Assess for Plasmodium parasites.
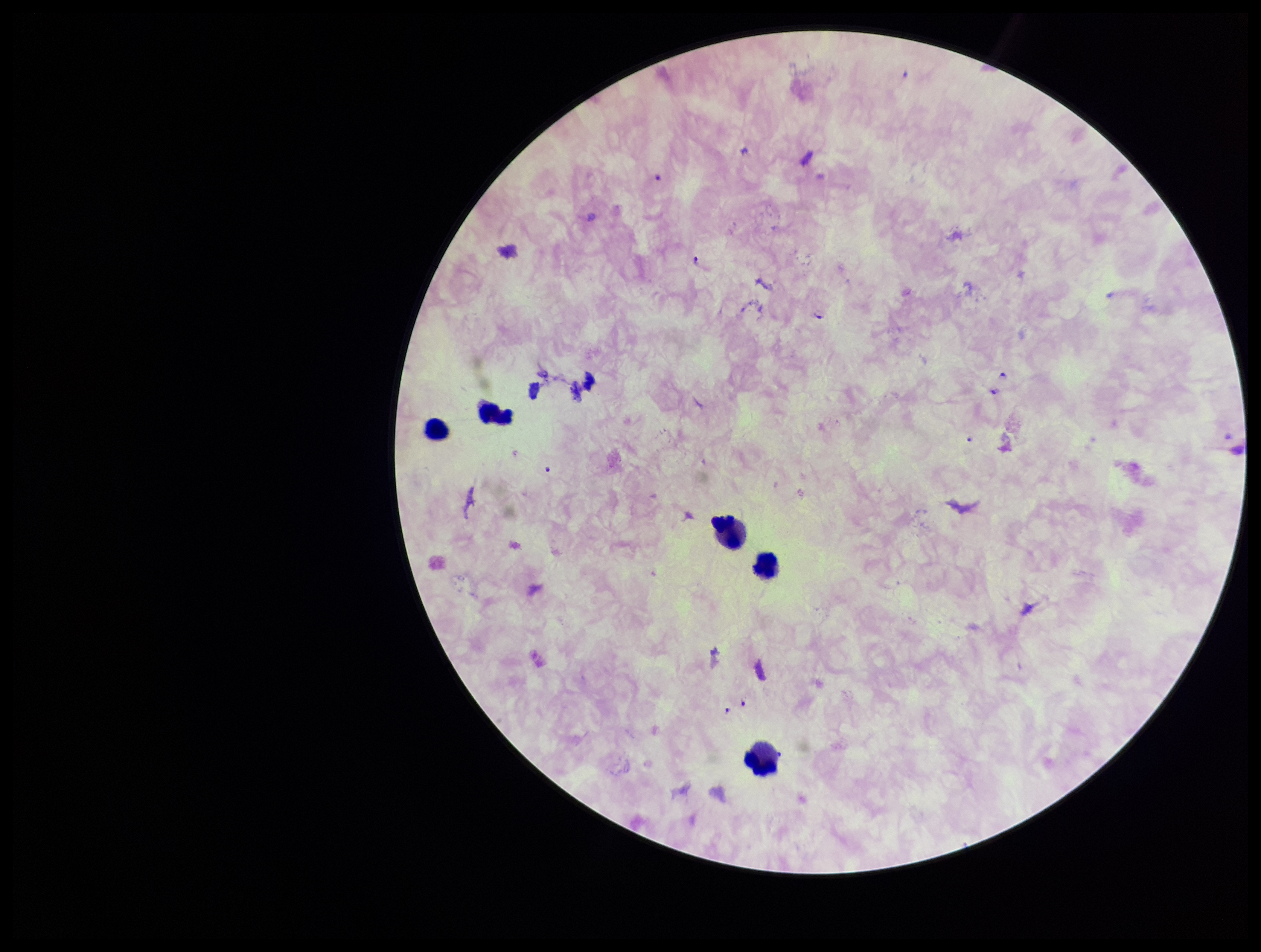

Detected.

Preparation: thick smear. Species reported for this patient: Plasmodium falciparum. Patient malaria status: infected. Leukocyte count: 5. Image is 1261×952 pixels. Photographed through the microscope eyepiece with a smartphone camera. One field from this slide. Giemsa stain. Parasite count: 7.